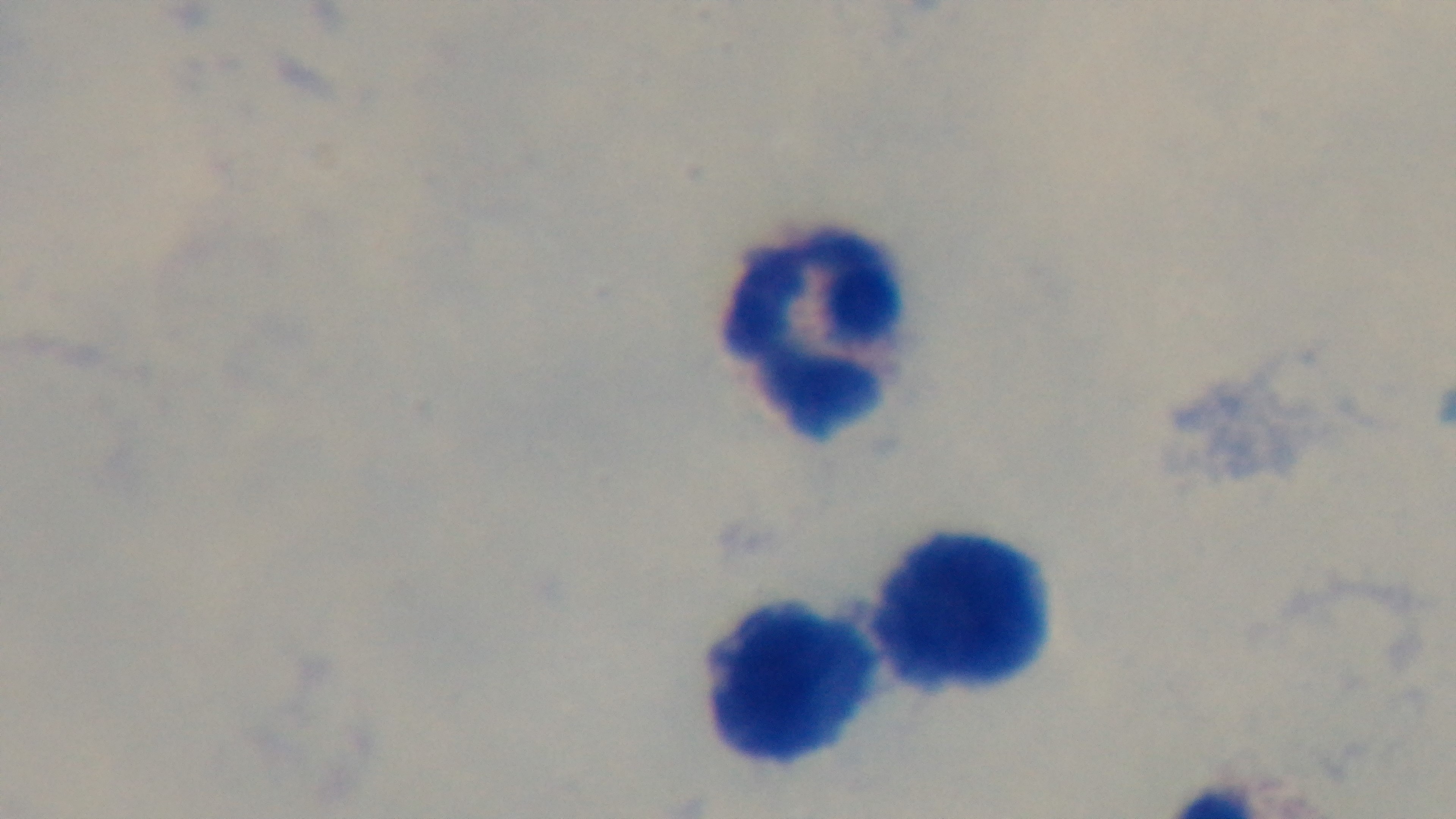

Captured with a mounted 4K digital camera. Preparation: thick smear. Single field of view. Light microscopy. Malaria status: negative. 100x oil-immersion objective. Giemsa stain.